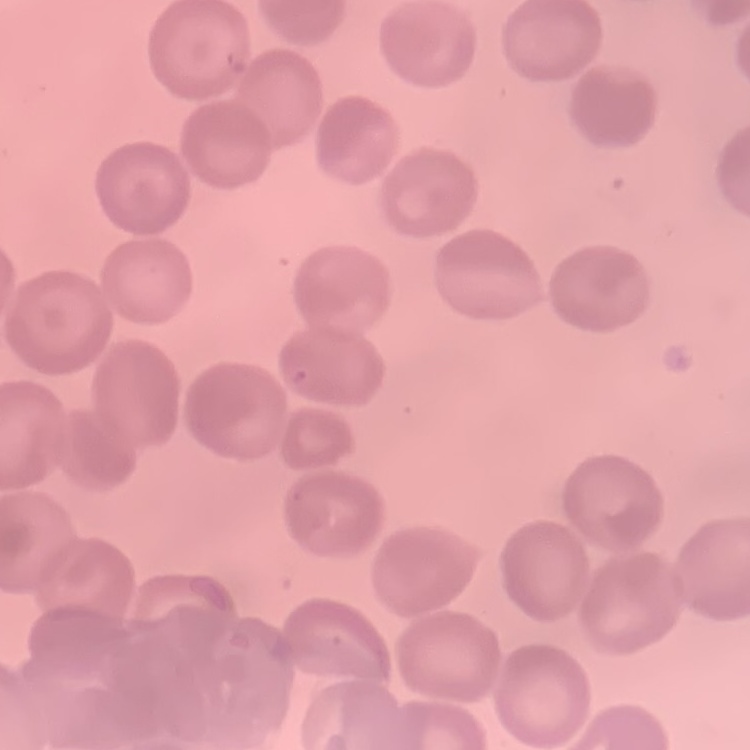
The erythrocytes exhibit no rouleaux formation. Thin peripheral smear. One tile cut from a larger photomicrograph. Field's or Giemsa stain.